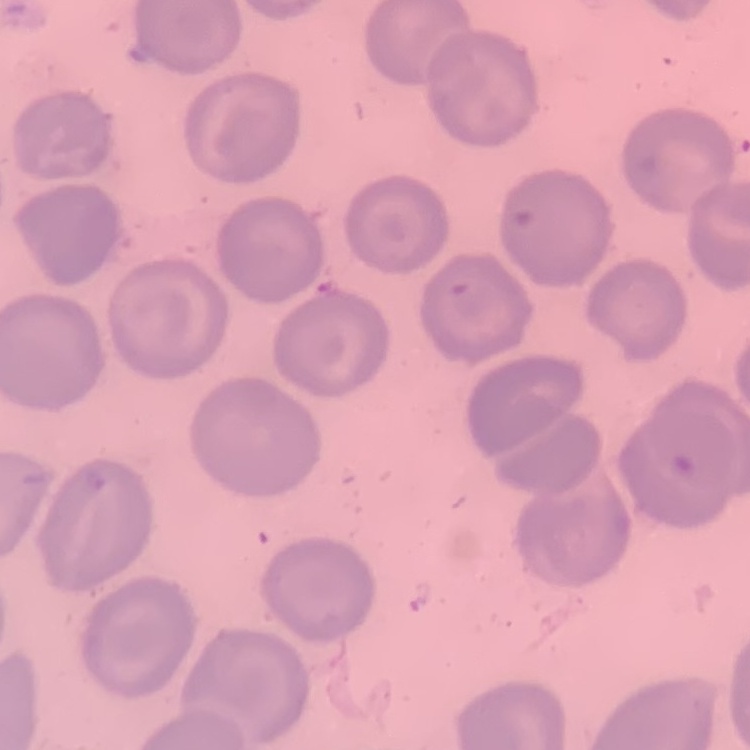

red blood cell morphology = no rouleaux formation
image type = square crop of a larger photomicrograph
preparation = thin peripheral smear
stain = Field's or Giemsa